Assess this cell for malaria.
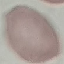
It is uninfected.

Automatically extracted cell patch, resized to 64 × 64 pixels. Acquired by smartphone through the microscope eyepiece. Giemsa-stained preparation. Thin blood smear.